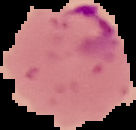
Result: Plasmodium parasites identified. Image is 136×130 pixels. Segmented cell region on a black background. From a thin blood film.